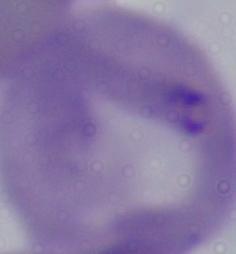

Summary:
  - Magnification: 1000x
  - Modality: photomicrograph
  - Identification: Babesia